Assess the morphology of the red blood cells.
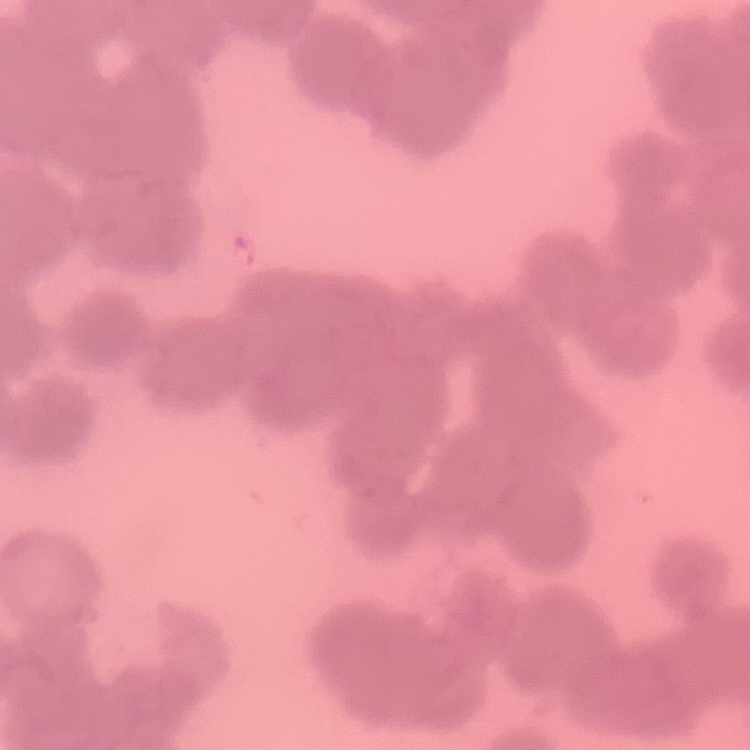

Rouleaux formation.

{
  "stain": "Field's or Giemsa",
  "image_type": "square crop of a larger photomicrograph",
  "preparation": "thin blood film"
}